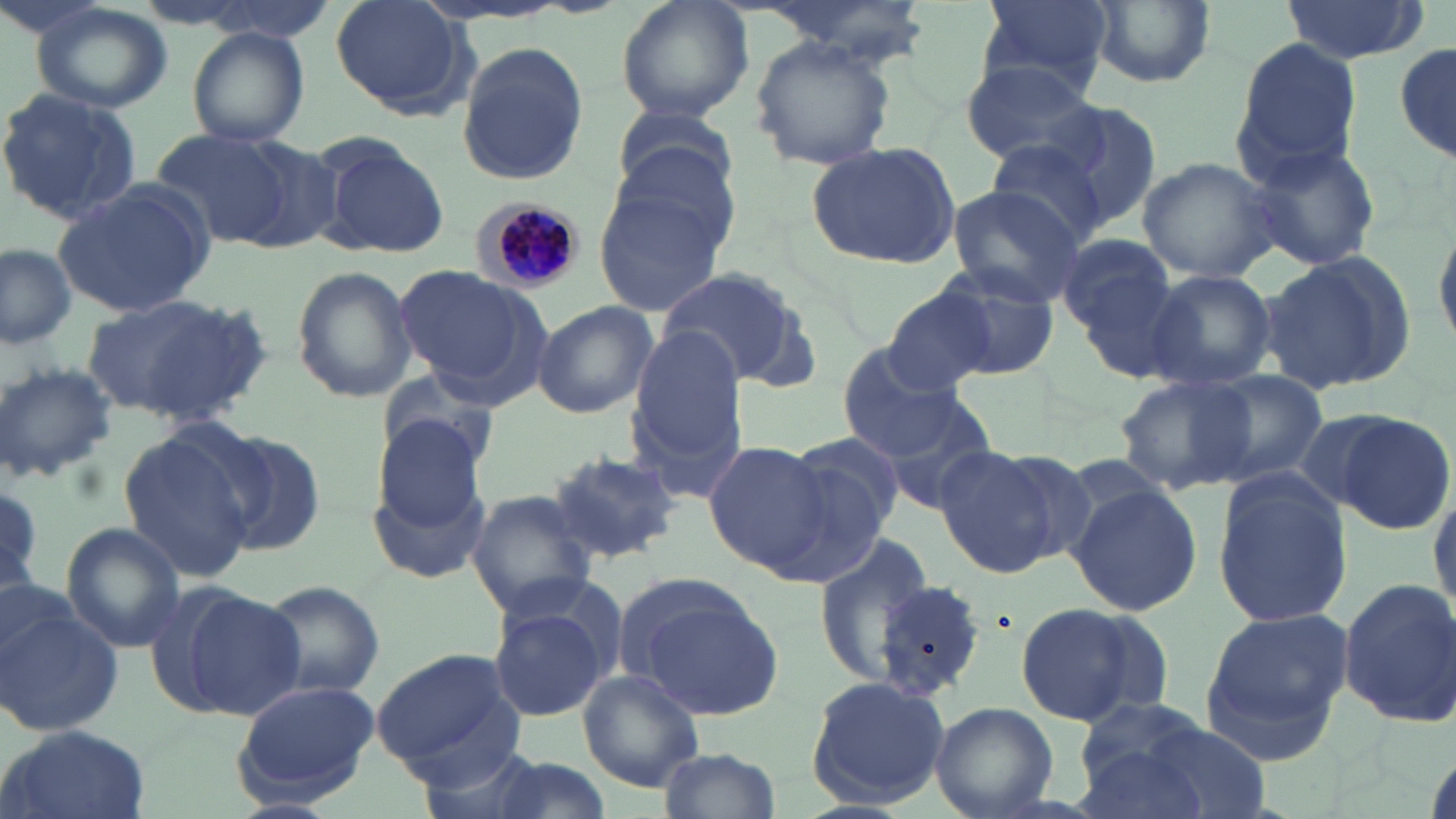 Approximate bounding boxes as named x1/y1/x2/y2 corners in pixels. Plasmodium malariae-infected red blood cell locations: (x1=474, y1=199, x2=587, y2=294). Uninfected red blood cell locations: (x1=329, y1=0, x2=474, y2=119), (x1=615, y1=0, x2=756, y2=124), (x1=759, y1=0, x2=933, y2=65), (x1=978, y1=0, x2=1114, y2=96), (x1=1276, y1=1, x2=1429, y2=64), (x1=1086, y1=2, x2=1214, y2=89), (x1=31, y1=3, x2=175, y2=114), (x1=186, y1=27, x2=311, y2=149), (x1=1393, y1=36, x2=1454, y2=167), (x1=1232, y1=37, x2=1363, y2=181), (x1=749, y1=38, x2=897, y2=172), (x1=455, y1=42, x2=589, y2=185), (x1=959, y1=57, x2=1102, y2=171), (x1=0, y1=85, x2=147, y2=227), (x1=1041, y1=98, x2=1168, y2=235), (x1=610, y1=104, x2=737, y2=201), (x1=152, y1=130, x2=297, y2=245), (x1=312, y1=131, x2=451, y2=258), (x1=806, y1=139, x2=961, y2=269), (x1=987, y1=139, x2=1111, y2=248), (x1=1242, y1=140, x2=1381, y2=272), (x1=1137, y1=157, x2=1280, y2=283), (x1=591, y1=178, x2=732, y2=319), (x1=50, y1=182, x2=217, y2=318), (x1=945, y1=186, x2=1083, y2=305), (x1=1429, y1=209, x2=1456, y2=354), (x1=1056, y1=234, x2=1177, y2=344), (x1=0, y1=242, x2=77, y2=351), (x1=1255, y1=248, x2=1420, y2=397), (x1=1069, y1=262, x2=1200, y2=385), (x1=929, y1=263, x2=1061, y2=379), (x1=393, y1=265, x2=547, y2=394), (x1=291, y1=266, x2=417, y2=403), (x1=655, y1=266, x2=814, y2=387), (x1=1145, y1=269, x2=1277, y2=391), (x1=882, y1=285, x2=993, y2=395), (x1=81, y1=292, x2=266, y2=426), (x1=532, y1=301, x2=658, y2=419), (x1=628, y1=327, x2=749, y2=462), (x1=837, y1=344, x2=967, y2=460), (x1=0, y1=359, x2=118, y2=484), (x1=376, y1=370, x2=506, y2=484), (x1=1194, y1=370, x2=1328, y2=487), (x1=1115, y1=374, x2=1256, y2=496), (x1=871, y1=390, x2=1000, y2=515), (x1=627, y1=400, x2=747, y2=509), (x1=1334, y1=411, x2=1454, y2=535), (x1=369, y1=416, x2=493, y2=532), (x1=204, y1=427, x2=330, y2=557), (x1=118, y1=429, x2=259, y2=581), (x1=783, y1=434, x2=907, y2=550), (x1=704, y1=441, x2=841, y2=578), (x1=932, y1=443, x2=1072, y2=577), (x1=547, y1=451, x2=685, y2=565), (x1=368, y1=463, x2=494, y2=589), (x1=1211, y1=470, x2=1353, y2=629), (x1=1429, y1=479, x2=1456, y2=622), (x1=1066, y1=481, x2=1203, y2=616), (x1=466, y1=491, x2=598, y2=619), (x1=60, y1=523, x2=187, y2=651), (x1=814, y1=529, x2=933, y2=689), (x1=622, y1=578, x2=786, y2=721), (x1=1337, y1=578, x2=1456, y2=729), (x1=257, y1=579, x2=385, y2=699), (x1=874, y1=580, x2=987, y2=701), (x1=174, y1=585, x2=307, y2=721), (x1=484, y1=594, x2=617, y2=723), (x1=1013, y1=603, x2=1162, y2=726), (x1=0, y1=604, x2=125, y2=737), (x1=1199, y1=607, x2=1355, y2=761), (x1=372, y1=649, x2=523, y2=775), (x1=577, y1=669, x2=706, y2=793), (x1=805, y1=675, x2=952, y2=808), (x1=231, y1=677, x2=377, y2=807), (x1=1075, y1=697, x2=1209, y2=806), (x1=930, y1=702, x2=1056, y2=817), (x1=0, y1=725, x2=152, y2=819), (x1=414, y1=738, x2=549, y2=819), (x1=659, y1=746, x2=780, y2=819). Slide-level diagnosis: Plasmodium malariae. Thin blood smear. 1000x magnification. May-Grünwald-Giemsa-stained preparation. Image is 1456×819 pixels. Light microscopy. One field of a larger specimen.